Identify the parasite.
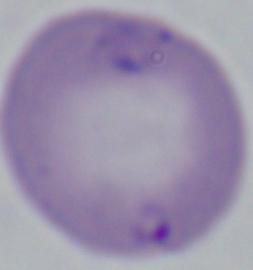

Babesia.

magnification = 1000x
modality = micrograph